Assess the background quality.
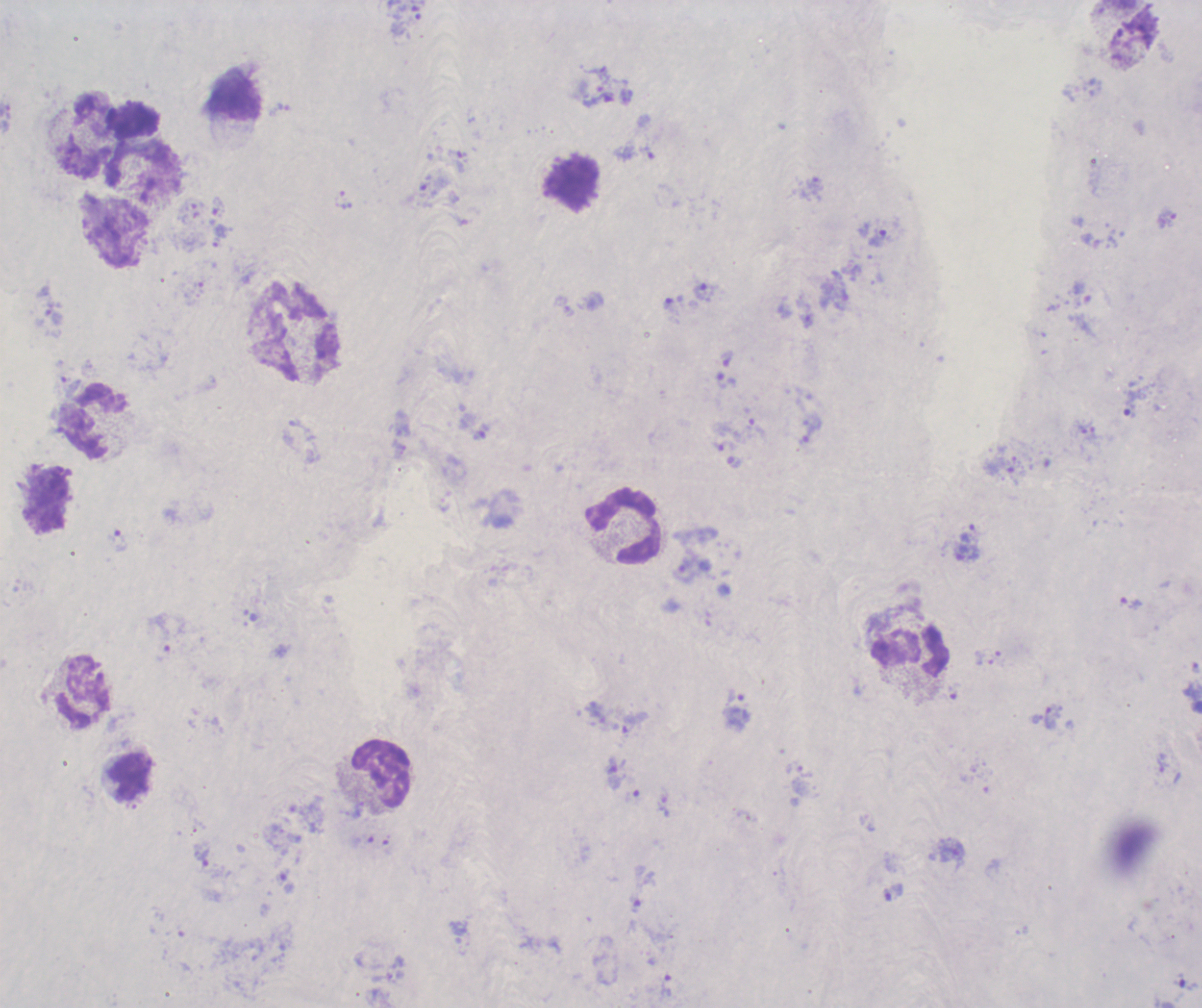
Poor.

Approximate object centers, in pixels from the top-left corner. Trophozoite locations: (x=457, y=161), (x=1166, y=219), (x=881, y=237), (x=704, y=291), (x=726, y=359), (x=726, y=381), (x=725, y=446), (x=117, y=540), (x=685, y=571), (x=1131, y=603), (x=1051, y=716), (x=635, y=722), (x=614, y=775), (x=203, y=857). Leukocyte locations: (x=235, y=98), (x=87, y=134), (x=144, y=173), (x=574, y=182), (x=114, y=233), (x=295, y=330), (x=92, y=422), (x=47, y=499), (x=624, y=526), (x=910, y=650), (x=83, y=689), (x=381, y=773), (x=130, y=777). Result: Plasmodium parasites identified. One field from this slide. Previously used in an actual diagnosis. Romanowsky-stained preparation. Image is 1202×1008 pixels. Thick smear of blood. 100x magnification.